Classify this cell by malaria status.
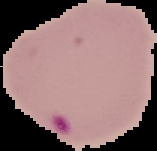
It is parasitized.

Summary:
  - Preparation: thin blood film
  - Image type: cell region segmented out of the field of view; surrounding area masked to black
  - Image size: 157×151 pixels